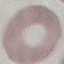

Result: no malaria parasites seen. Giemsa-stained preparation. Acquired by smartphone through the microscope eyepiece. Thin blood film. Automatically extracted cell patch, resized to 64 × 64 pixels.